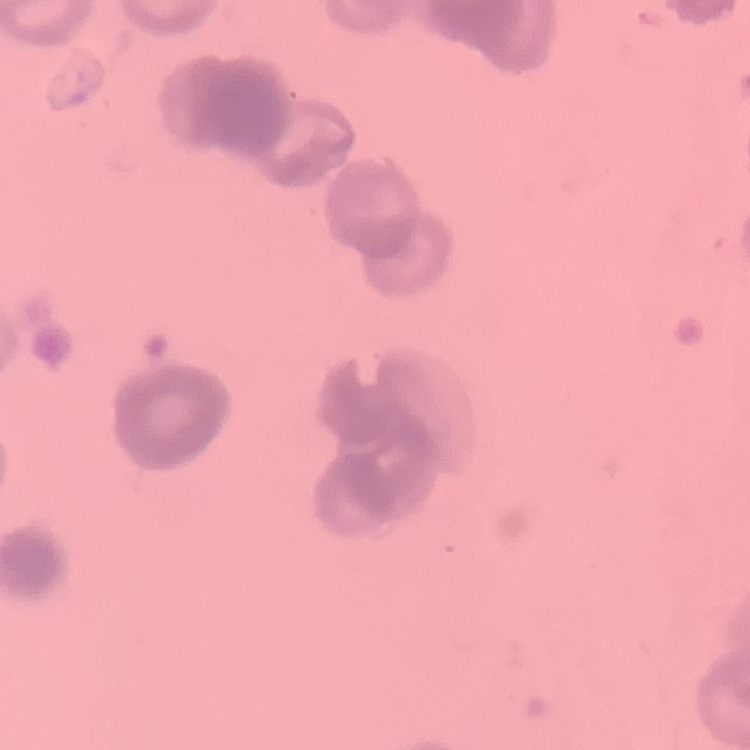

{
  "erythrocyte_morphology": "rouleaux formation",
  "preparation": "thin blood film",
  "stain": "Field's or Giemsa",
  "image_type": "square crop of a larger photomicrograph"
}